Name the blood parasite species.
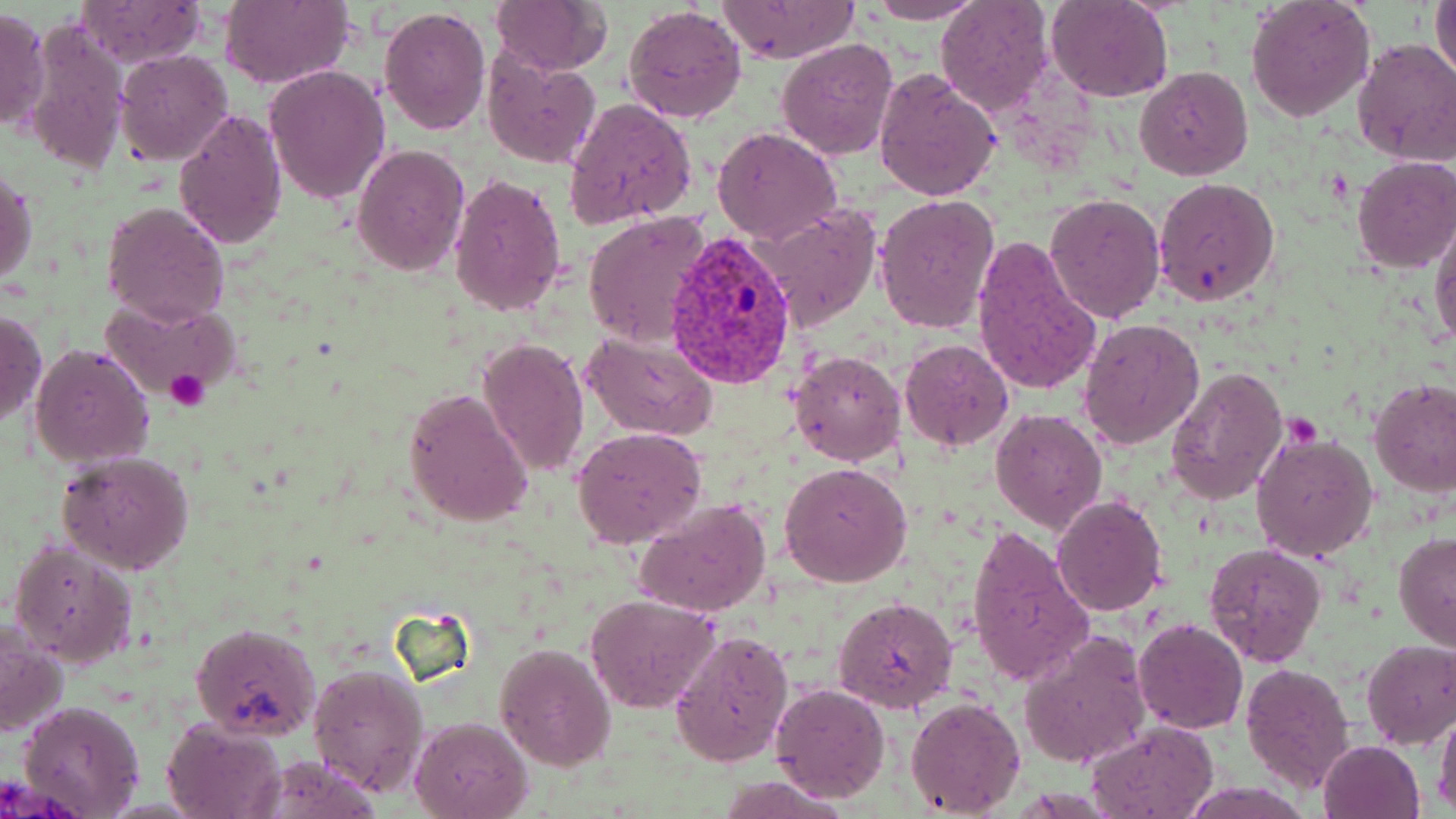
Plasmodium vivax.

preparation: thin blood film
plasmodium_vivax_infected_red_blood_cell_locations: 'approximate bounding boxes as [x1, y1, x2, y2] in pixels: [665, 230, 799, 390]'
field_of_view: one of a larger specimen
stain: May-Grünwald-Giemsa
platelet_locations: 'approximate bounding boxes as [x1, y1, x2, y2] in pixels: [165, 368, 209, 412], [1284, 416, 1320, 447]'
magnification: 1000x
modality: optical microscopy
uninfected_red_blood_cell_locations: 'approximate bounding boxes as [x1, y1, x2, y2] in pixels: [860, 0, 987, 24], [1246, 0, 1375, 121], [1431, 0, 1456, 83], [74, 1, 207, 68], [220, 1, 353, 90], [488, 1, 614, 76], [717, 1, 858, 64], [935, 1, 1054, 117], [1046, 1, 1173, 102], [622, 4, 747, 126], [377, 5, 491, 137], [0, 8, 51, 132], [22, 18, 131, 175], [777, 38, 899, 159], [1352, 39, 1456, 164], [114, 50, 232, 163], [480, 52, 603, 168], [264, 65, 391, 206], [873, 67, 1001, 201], [1135, 67, 1253, 182], [564, 97, 697, 228], [172, 107, 288, 251], [713, 127, 841, 243], [351, 143, 469, 276], [1352, 155, 1456, 273], [1, 170, 37, 287], [447, 173, 568, 317], [1152, 176, 1279, 307], [1045, 193, 1165, 323], [874, 194, 1002, 336], [101, 200, 229, 327], [756, 203, 881, 330], [581, 210, 712, 347], [1430, 215, 1456, 350], [972, 237, 1101, 396], [100, 297, 242, 405], [0, 307, 46, 430], [1078, 317, 1204, 450], [581, 328, 718, 441], [479, 337, 589, 477], [899, 339, 1014, 452], [30, 344, 154, 466], [789, 350, 907, 466], [1166, 366, 1289, 506], [1369, 378, 1456, 496], [404, 388, 533, 528], [991, 408, 1105, 534], [572, 427, 708, 547], [1251, 429, 1379, 563], [58, 452, 195, 575], [780, 463, 912, 587], [1052, 494, 1168, 615], [632, 498, 774, 620], [967, 523, 1095, 685], [1392, 532, 1456, 655], [9, 540, 138, 666], [1203, 542, 1326, 665], [585, 594, 719, 712], [833, 595, 958, 715], [1135, 617, 1247, 733], [0, 619, 68, 737], [191, 622, 321, 740], [669, 629, 794, 766], [1019, 630, 1152, 770], [1361, 639, 1456, 748], [495, 643, 615, 770], [308, 661, 431, 798], [1242, 662, 1354, 792], [770, 684, 890, 802], [906, 697, 1026, 817], [18, 700, 146, 817], [1435, 706, 1456, 814], [410, 716, 532, 819], [163, 719, 288, 819], [1086, 721, 1218, 818], [1318, 739, 1425, 819], [257, 755, 383, 818]'
image_size: 1456×819 pixels